Give the position of every Plasmodium parasite visible.
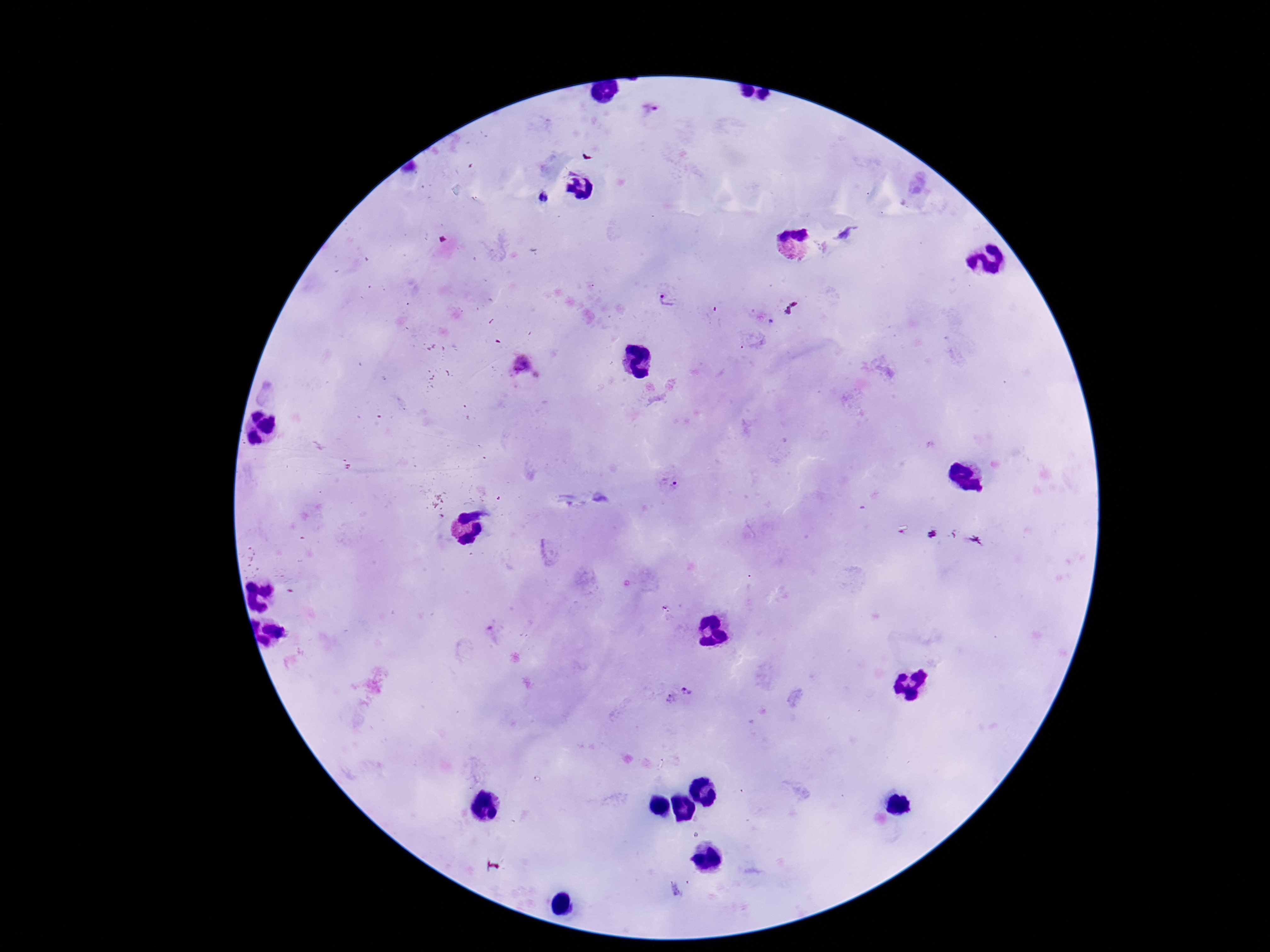
Approximate centers as [x, y] in pixels.
Plasmodium parasites: [650, 108], [543, 197], [845, 232], [669, 298], [522, 364], [670, 481], [687, 690], [670, 699].

capture = smartphone camera through the microscope eyepiece
field of view = one from this slide
patient malaria status = positive
image size = 1270×952 pixels
preparation = thick peripheral-blood smear
stain = Giemsa
magnification = 100x